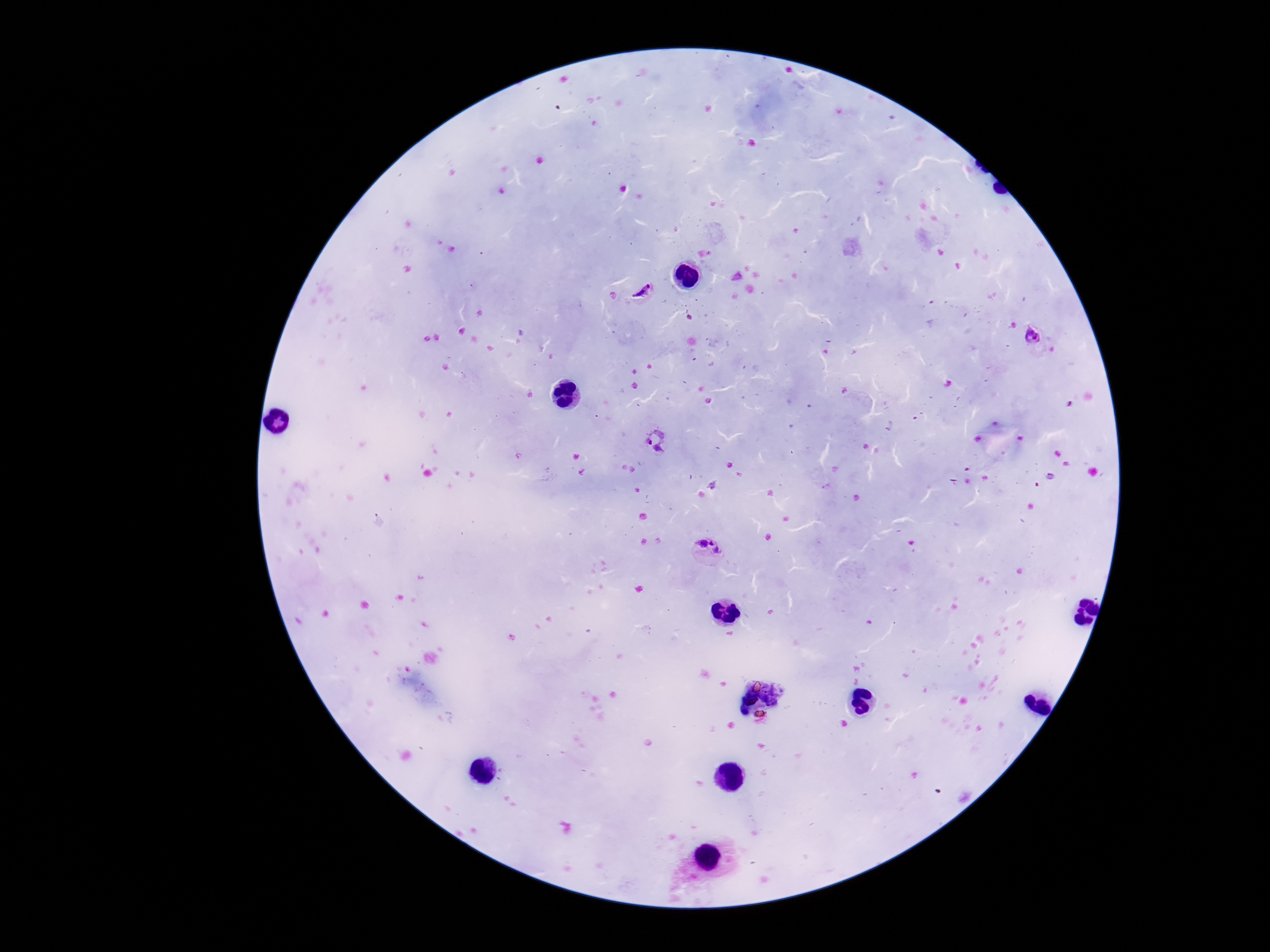
Approximate centers as {x, y} in pixels.
Summary:
  - Plasmodium parasite locations: {642, 291}, {1033, 336}, {656, 441}, {708, 551}
  - Image size: 1270×952 pixels
  - Capture: smartphone camera through the microscope eyepiece
  - Magnification: 100x
  - Field of view: one from this slide
  - Patient malaria status: positive
  - Preparation: thick peripheral-blood smear
  - Stain: Giemsa